State the blood parasite species.
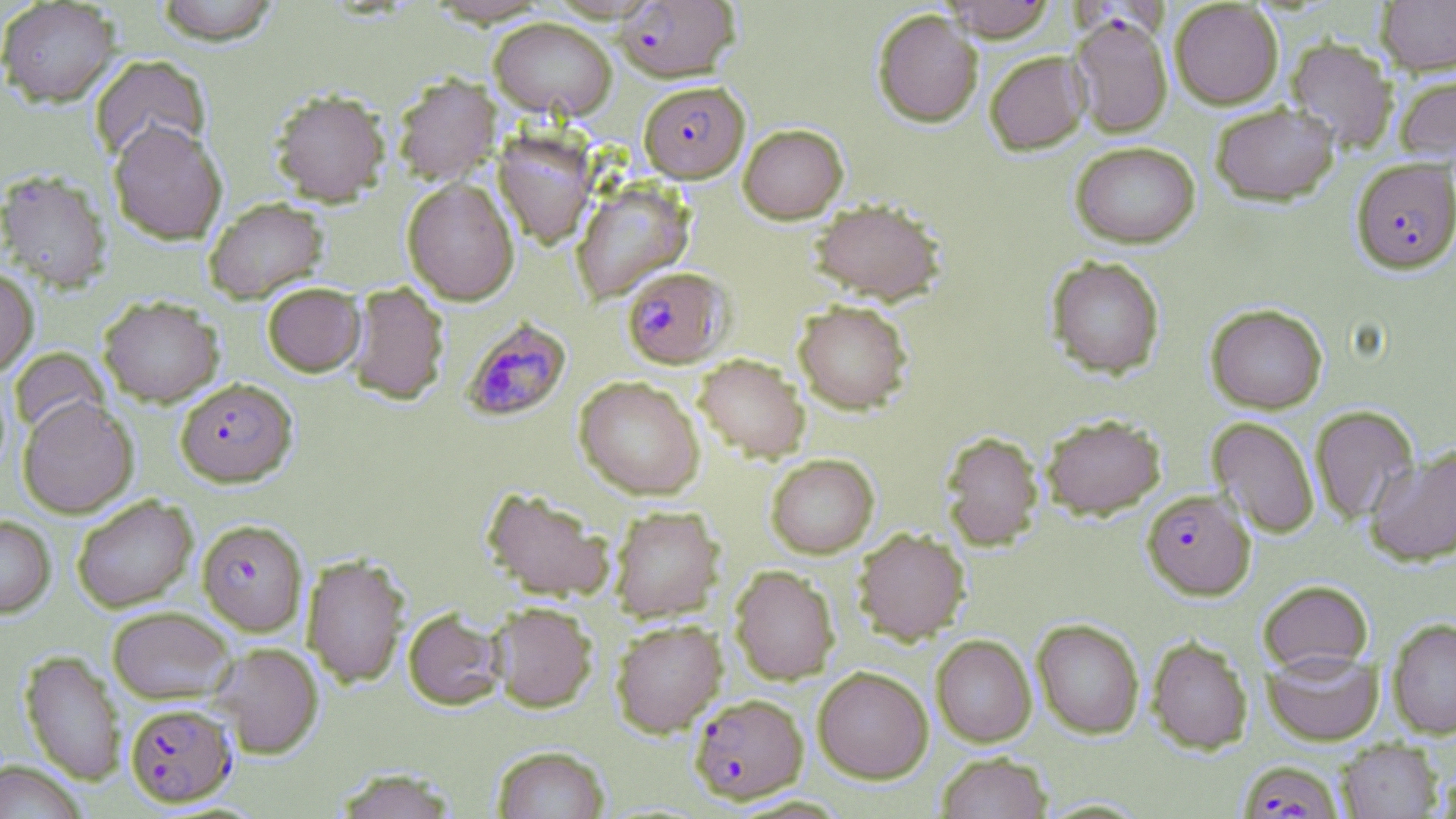
Plasmodium falciparum.

Approximate bounding boxes as [x1, y1, x2, y2] in pixels. Uninfected red blood cell locations: [154, 0, 281, 45], [941, 0, 1057, 41], [1377, 0, 1456, 75], [0, 1, 121, 107], [1170, 1, 1283, 109], [872, 9, 983, 127], [489, 16, 617, 120], [1286, 37, 1398, 153], [984, 50, 1090, 154], [89, 54, 211, 164], [392, 73, 501, 185], [1394, 74, 1456, 163], [270, 88, 390, 205], [1210, 102, 1339, 206], [108, 121, 227, 244], [738, 123, 848, 223], [493, 130, 598, 247], [1070, 141, 1200, 248], [0, 169, 112, 291], [402, 177, 519, 305], [571, 181, 694, 304], [203, 197, 329, 303], [809, 198, 946, 304], [1046, 255, 1165, 378], [0, 267, 38, 377], [345, 281, 449, 405], [262, 282, 366, 377], [98, 295, 223, 407], [793, 299, 913, 414], [1206, 303, 1328, 414], [10, 347, 109, 438], [694, 354, 810, 462], [575, 376, 704, 499], [18, 397, 139, 518], [1309, 404, 1420, 524], [1040, 413, 1166, 519], [1207, 416, 1319, 539], [941, 430, 1044, 549], [1365, 445, 1456, 566], [765, 453, 879, 558], [481, 486, 614, 602], [71, 494, 198, 612], [609, 504, 724, 622], [0, 515, 56, 617], [853, 527, 970, 644], [302, 554, 410, 688], [730, 565, 840, 684], [1257, 579, 1373, 674], [490, 602, 598, 713], [107, 605, 236, 704], [403, 608, 505, 711], [1387, 617, 1456, 739], [1032, 618, 1145, 738], [610, 619, 726, 737], [931, 634, 1036, 747], [1146, 635, 1253, 754], [212, 642, 323, 759], [1263, 648, 1382, 745], [20, 650, 125, 784], [813, 665, 933, 783], [1337, 739, 1442, 818], [492, 745, 610, 819], [936, 752, 1052, 819], [1, 761, 86, 819], [333, 767, 458, 818]. Plasmodium falciparum-infected red blood cell locations: [614, 0, 739, 83], [1069, 13, 1173, 138], [638, 80, 749, 182], [1351, 157, 1456, 272], [621, 266, 731, 368], [462, 317, 571, 421], [175, 378, 297, 486], [1142, 489, 1255, 599], [197, 519, 308, 636], [689, 693, 808, 804], [124, 702, 237, 807], [1237, 760, 1344, 818]. Single field of view. 1000x magnification. May-Grünwald-Giemsa stain. Thin blood smear. Image is 1456×819 pixels. Optical microscopy.